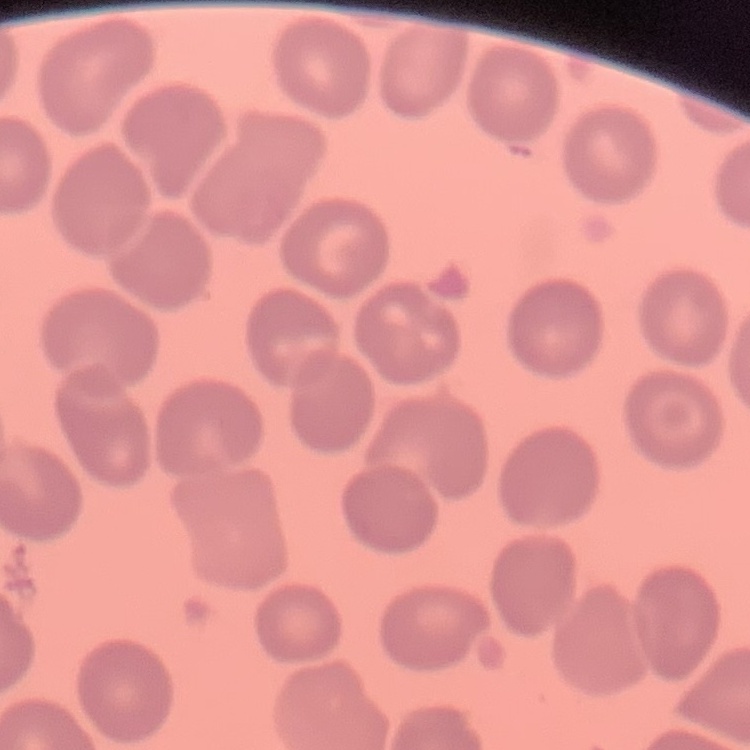

red blood cell morphology = no rouleaux formation
preparation = thin blood smear
image type = square crop of a larger photomicrograph
stain = Field's or Giemsa